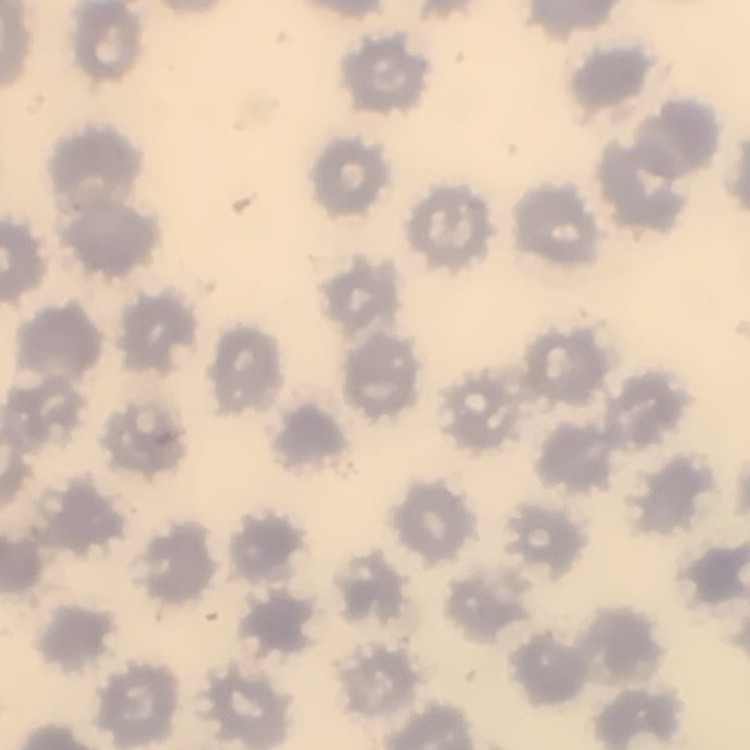

erythrocyte_morphology: no rouleaux formation
stain: Field's or Giemsa
image_type: one tile cut from a larger photomicrograph
preparation: thin blood smear